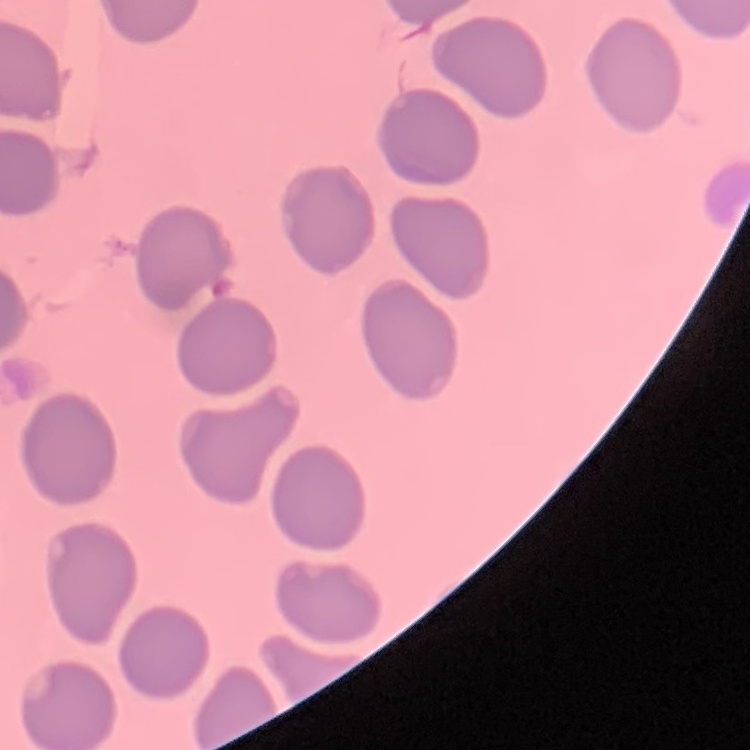
{
  "red_blood_cell_morphology": "no rouleaux formation",
  "stain": "Field's or Giemsa",
  "image_type": "one tile cut from a larger photomicrograph",
  "preparation": "thin blood film"
}